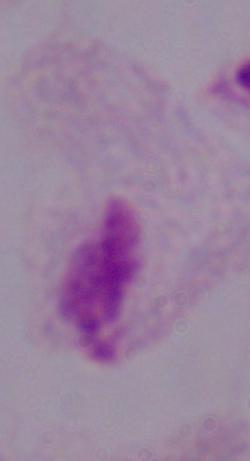

Micrograph. Captured at 1000x magnification. A trichomonad is shown.